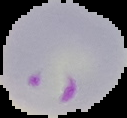

Summary:
  - Image type: segmented cell region on a black background
  - Preparation: thin blood film
  - Malaria status: parasitized
  - Image size: 127×118 pixels